Identify the parasite.
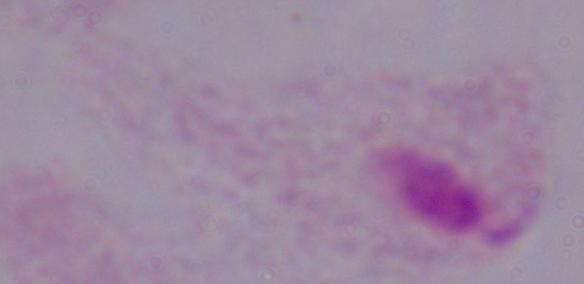

This is a trichomonad.

Summary:
  - Magnification: 1000x
  - Modality: micrograph